Locate every malaria parasite.
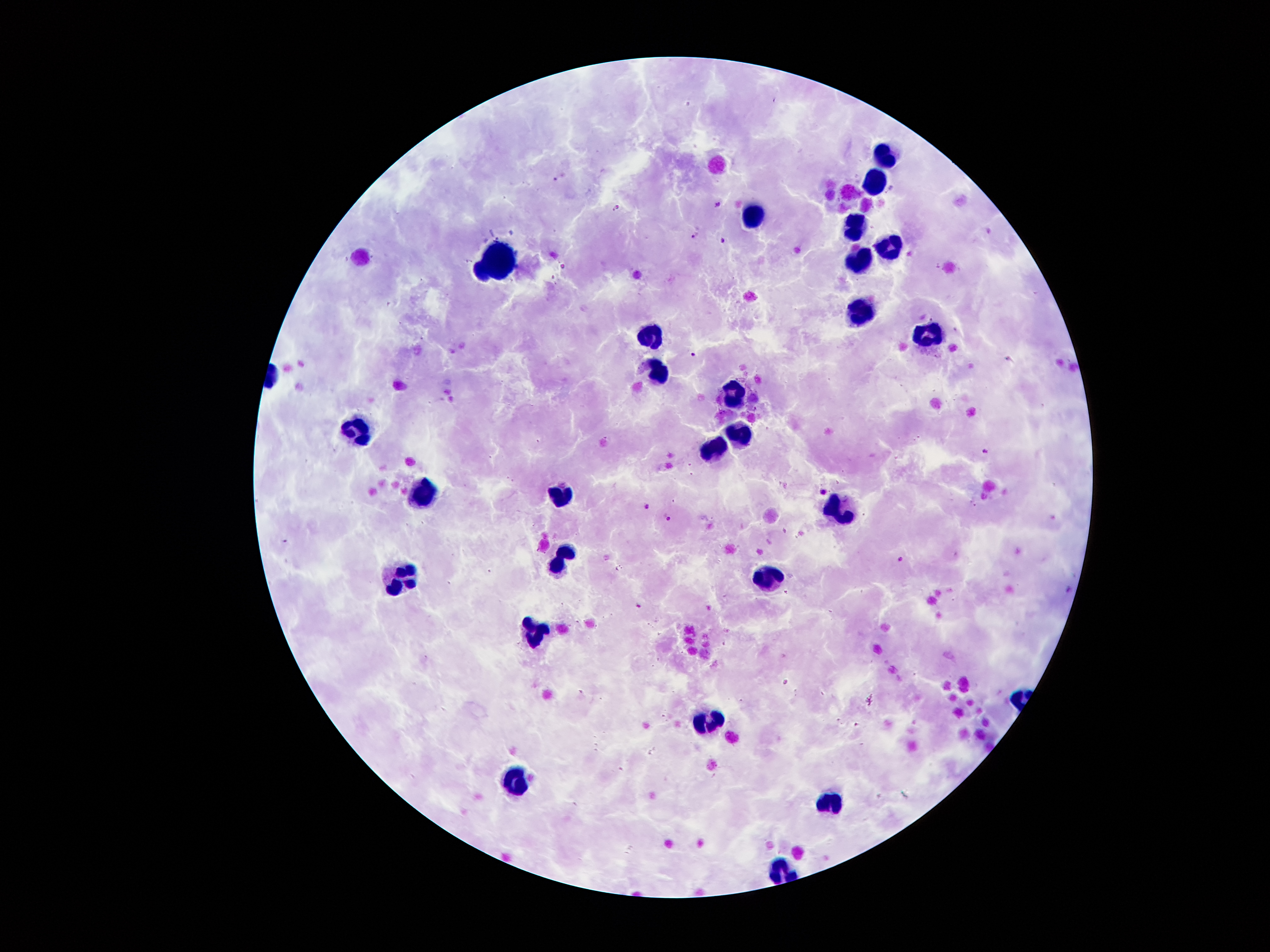
Approximate object centers, in pixels from the top-left corner.
Malaria parasites: (x=719, y=205), (x=617, y=207), (x=694, y=237), (x=724, y=240), (x=693, y=354), (x=756, y=408), (x=985, y=453), (x=824, y=492), (x=648, y=507), (x=668, y=517), (x=901, y=559), (x=639, y=606).

leukocyte locations = (x=885, y=150), (x=876, y=179), (x=748, y=218), (x=855, y=226), (x=888, y=242), (x=501, y=255), (x=856, y=260), (x=863, y=308), (x=648, y=333), (x=924, y=336), (x=657, y=367), (x=735, y=396), (x=354, y=425), (x=741, y=431), (x=711, y=450), (x=425, y=486), (x=557, y=496), (x=835, y=507), (x=554, y=562), (x=404, y=573), (x=772, y=578), (x=530, y=635), (x=708, y=715), (x=515, y=785), (x=830, y=799)
capture = smartphone camera through the microscope eyepiece
patient malaria status = positive for Plasmodium falciparum
magnification = 100x
stain = Giemsa
preparation = thick blood smear
image size = 1270×952 pixels
field of view = single